Locate and identify every blood parasite.
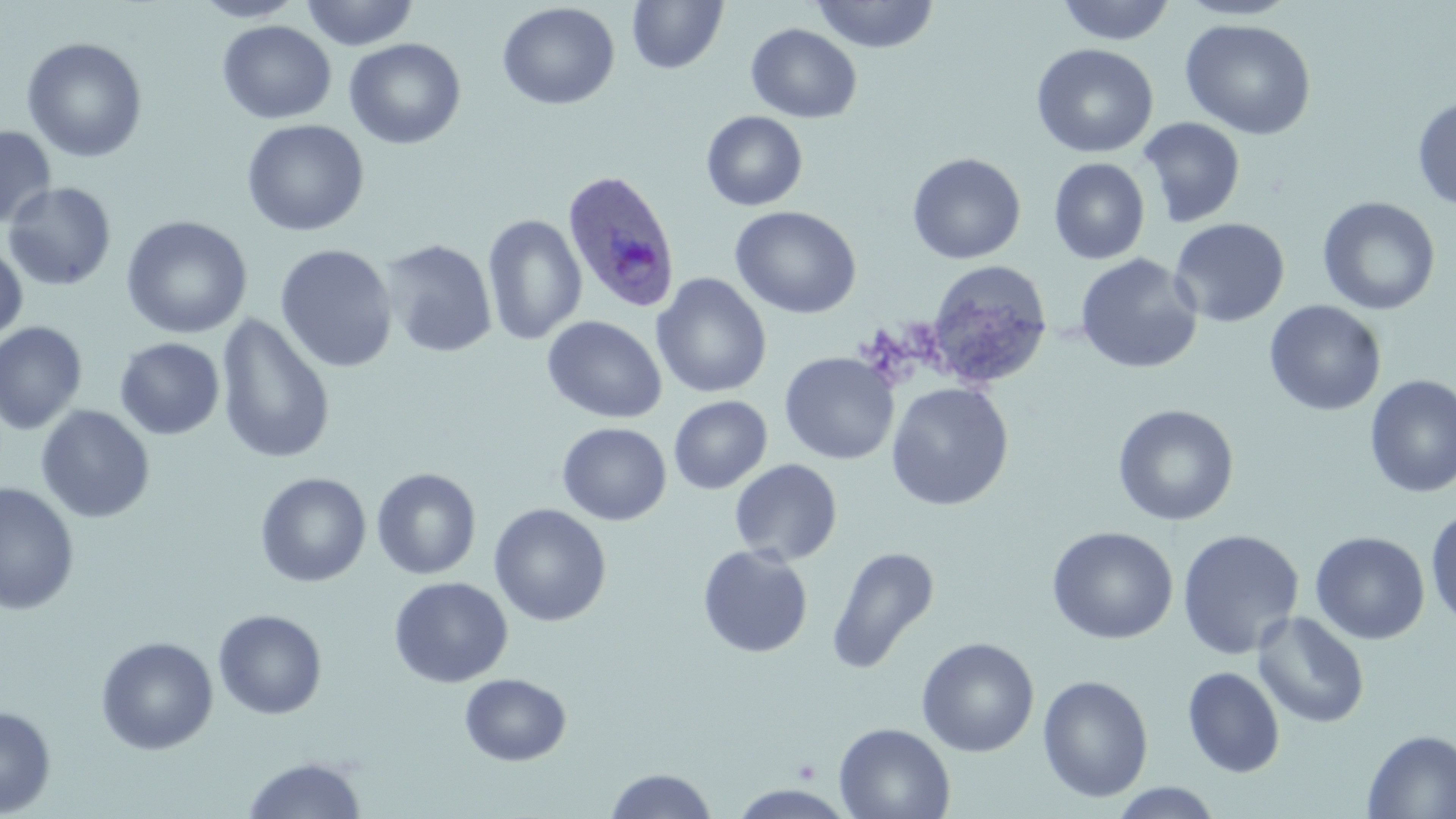
Approximate bounding boxes as (x1,y1)-(x2,y2) corner pairs in pixels.
Plasmodium ovale-infected red blood cells: (561,169)-(682,315).
No Plasmodium falciparum, Plasmodium malariae, Plasmodium vivax, Babesia divergens, or Trypanosoma brucei observed.

Platelet locations: (793,758)-(820,782). Uninfected red blood cell locations: (190,0)-(306,22), (300,0)-(419,50), (627,0)-(728,74), (811,0)-(939,53), (1055,0)-(1176,46), (1176,0)-(1300,21), (497,2)-(620,110), (1180,18)-(1317,140), (217,20)-(337,124), (746,23)-(862,123), (21,37)-(148,163), (344,38)-(466,150), (1031,43)-(1158,158), (1412,94)-(1456,212), (701,110)-(808,211), (1137,117)-(1246,228), (241,119)-(370,237), (0,125)-(57,230), (907,152)-(1026,264), (1049,158)-(1150,265), (3,182)-(117,291), (1317,196)-(1441,316), (730,205)-(862,319), (482,214)-(587,346), (120,215)-(253,339), (1169,218)-(1290,328), (379,239)-(497,358), (0,242)-(28,342), (275,244)-(398,373), (1074,254)-(1203,374), (925,259)-(1053,390), (651,273)-(772,399), (1264,300)-(1387,416), (215,313)-(336,466), (542,315)-(667,423), (0,321)-(88,435), (115,337)-(225,439), (779,351)-(898,464), (1364,374)-(1456,498), (885,382)-(1013,511), (669,395)-(772,494), (1112,404)-(1239,526), (36,405)-(155,523), (557,422)-(671,526), (730,459)-(843,565), (371,468)-(481,579), (255,472)-(371,587), (0,482)-(80,617), (489,503)-(612,627), (1425,507)-(1456,631), (1046,526)-(1178,645), (1176,529)-(1304,660), (1310,531)-(1430,645), (697,544)-(814,658), (826,545)-(940,675), (389,577)-(513,688), (213,609)-(328,720), (1251,611)-(1370,728), (95,636)-(218,755), (916,637)-(1040,757), (1181,666)-(1286,778), (459,672)-(572,767), (1038,674)-(1154,803), (0,705)-(56,817), (833,723)-(956,819), (1362,729)-(1456,818), (242,756)-(368,818), (603,768)-(719,818), (1107,782)-(1224,818). Slide-level diagnosis: Plasmodium ovale. Captured at 1000x magnification. Thin blood film. Optical microscopy. May-Grünwald-Giemsa-stained preparation. Image is 1456×819 pixels. One field of a larger specimen.